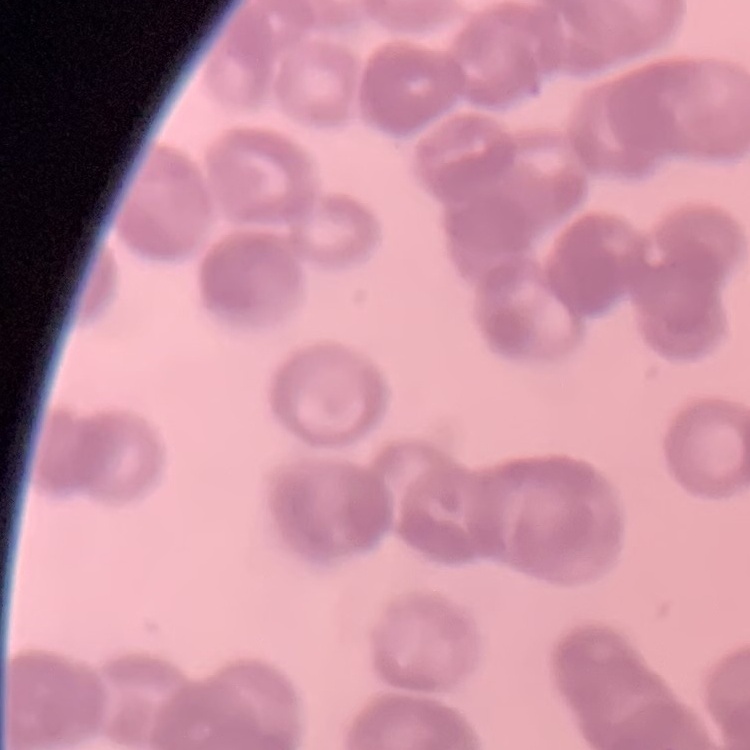
Summary:
  - Red blood cell morphology: rouleaux formation
  - Preparation: thin blood film
  - Stain: Field's or Giemsa
  - Image type: one tile cut from a larger photomicrograph